Look for Plasmodium parasites.
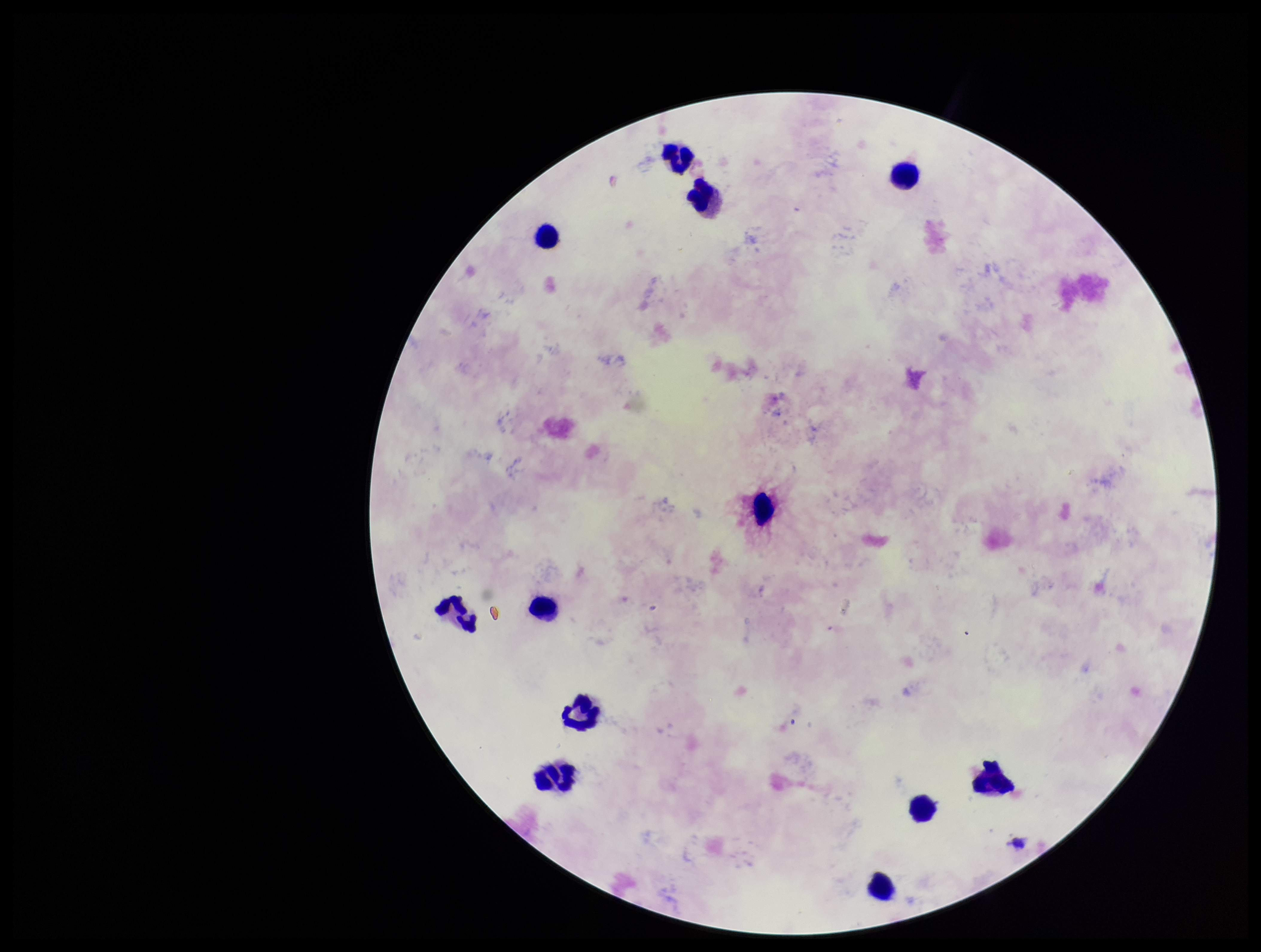
None seen.

Single field of view. Parasite count: 0. Patient malaria status: infected. Smartphone photograph taken through the eyepiece of a microscope. Preparation: thick blood smear. Leukocyte count: 12. Species reported for this patient: Plasmodium falciparum. Image is 1261×952 pixels. Giemsa stain.